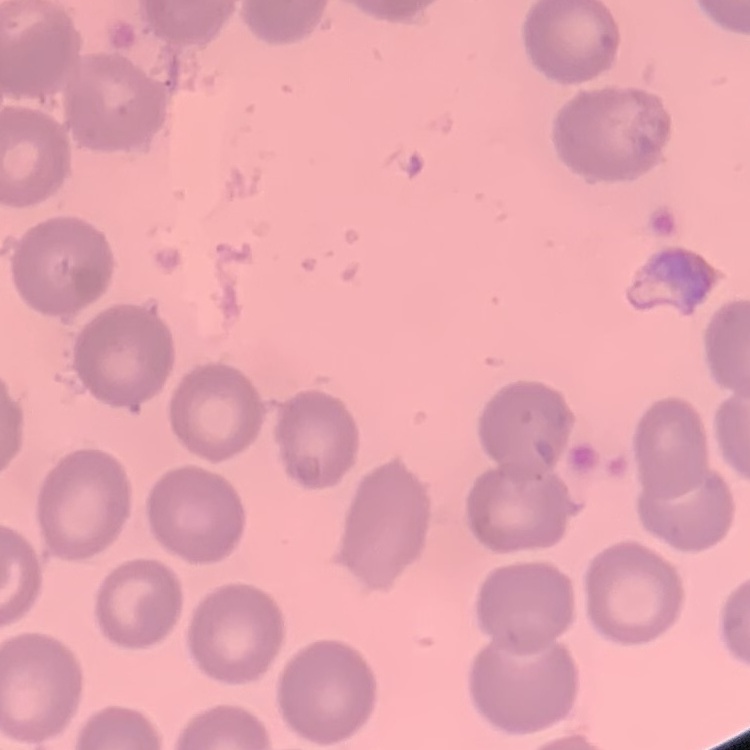

Summary:
  - Red blood cell morphology: no rouleaux formation
  - Preparation: thin peripheral smear
  - Stain: Field's or Giemsa
  - Image type: square crop of a larger photomicrograph